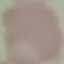

Summary:
  - Malaria status: uninfected
  - Image type: automatically extracted cell patch, resized to 64 × 64 pixels
  - Stain: Giemsa
  - Preparation: thin blood film
  - Capture: smartphone through the microscope eyepiece